Assess this cell for malaria.
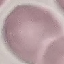

Uninfected.

capture = smartphone camera at the microscope eyepiece
stain = Giemsa
preparation = thin blood smear
image type = cell patch, automatically extracted from a larger field of view and resized to 64 × 64 pixels